Report the malaria status of this cell.
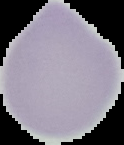
Uninfected.

From a thin blood smear. Image is 124×145 pixels. The area outside the segmented cell region is set to black.